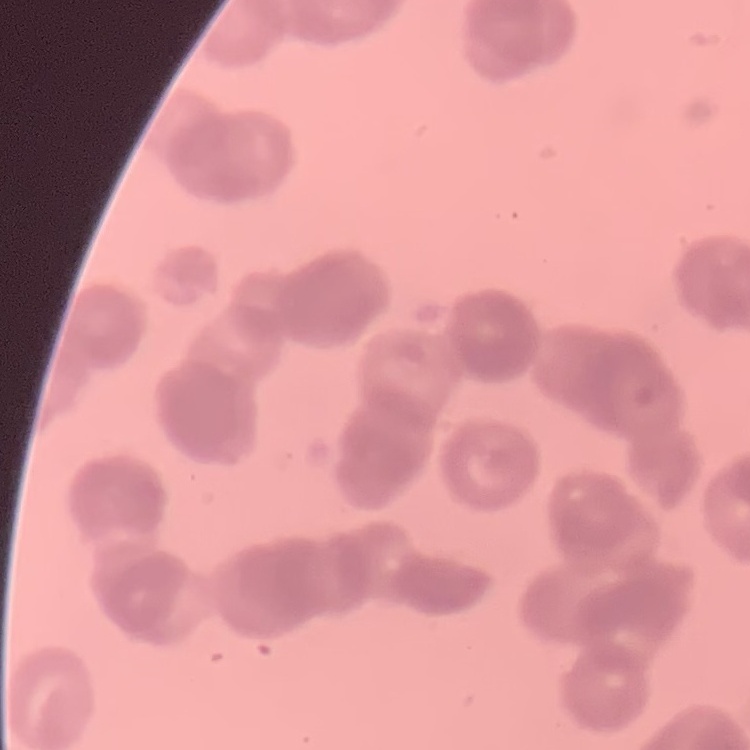

Summary:
  - Erythrocyte morphology: rouleaux formation
  - Image type: square crop of a larger photomicrograph
  - Stain: Field's or Giemsa
  - Preparation: thin blood film